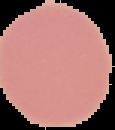

The area outside the segmented cell region is set to black. Result: no Plasmodium parasites detected. From a thin blood smear. Image is 115×130 pixels.